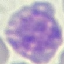
Summary:
  - Malaria status: parasitized
  - Stain: Giemsa
  - Image type: automatically extracted cell patch, resized to 64 × 64 pixels
  - Capture: smartphone camera at the microscope eyepiece
  - Preparation: thin blood film